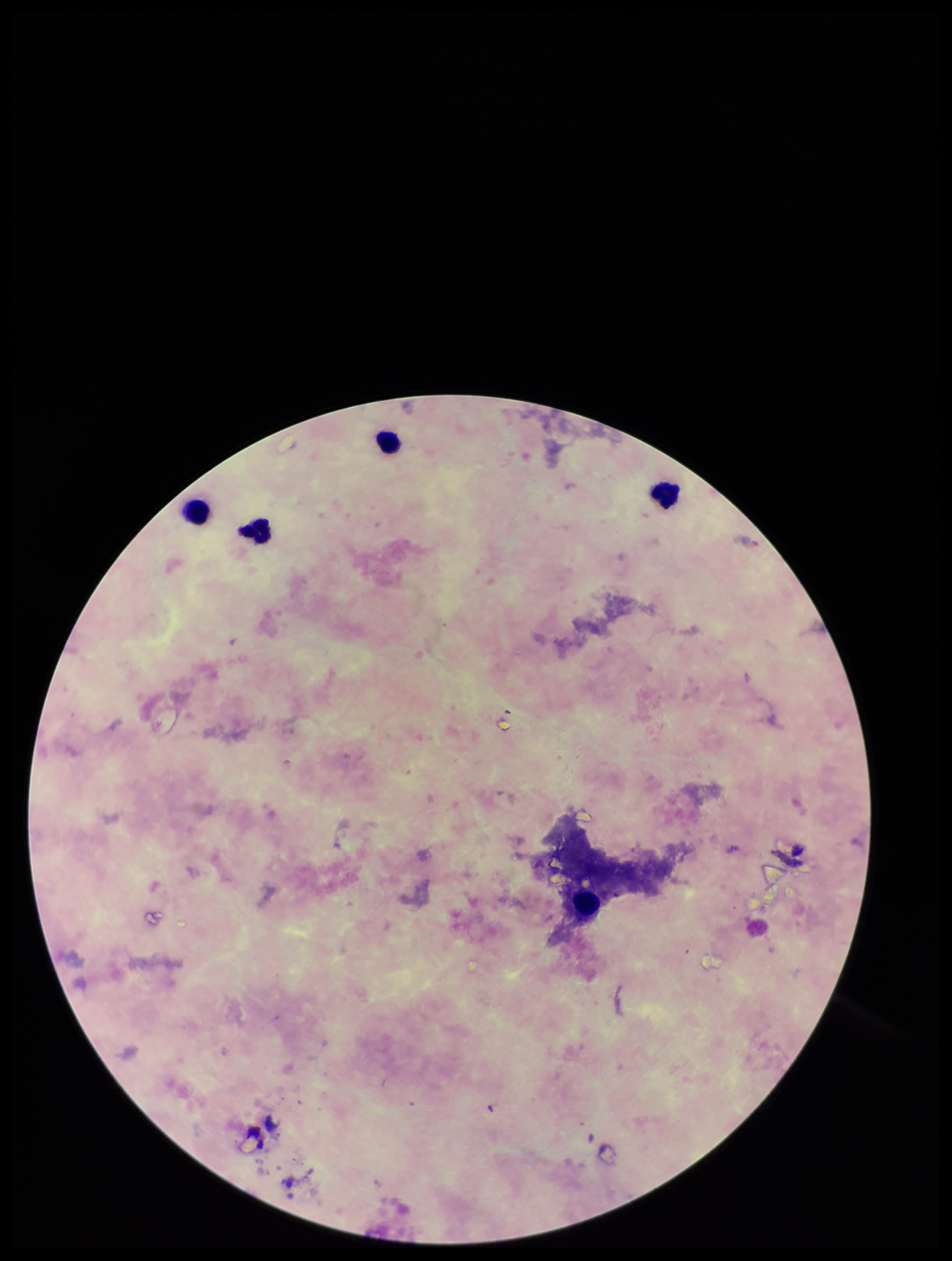
Smartphone photograph taken through the eyepiece of a microscope. Parasite count: 0. Patient malaria status: negative. Single field of view. Image is 952×1261 pixels. Preparation: thick. Leukocyte count: 5. Giemsa stain. Plasmodium parasites: none identified.